Assess this cell for malaria.
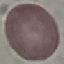
Uninfected.

Acquired by smartphone through the microscope eyepiece. Thin blood smear. Giemsa-stained preparation. Automatically extracted cell patch, resized to 64 × 64 pixels.